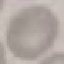

Malaria status: uninfected. Thin blood smear. Cell patch, automatically extracted from a larger field of view and resized to 64 × 64 pixels. Giemsa-stained preparation. Photographed with a smartphone camera at the microscope eyepiece.